Assess the morphology of the erythrocytes.
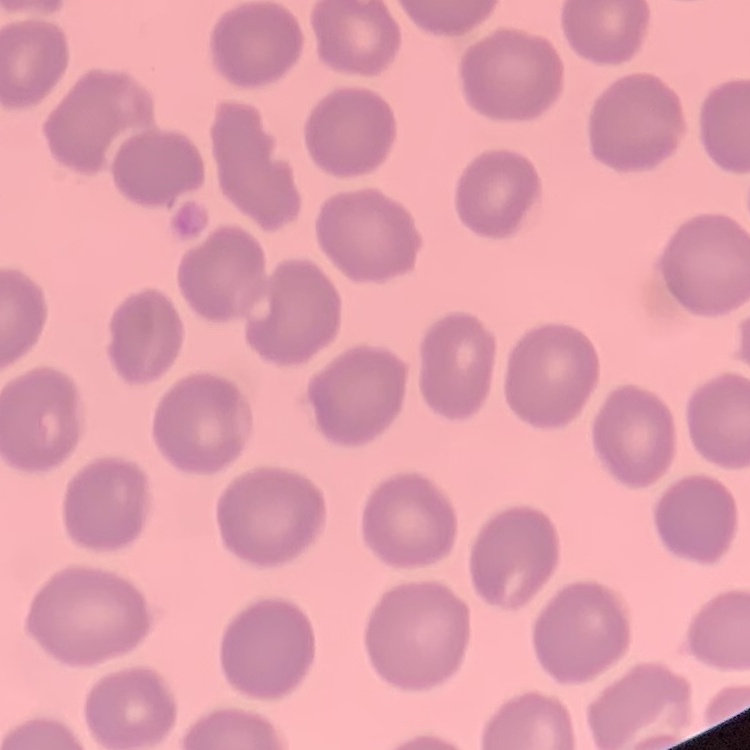

They show no rouleaux formation.

{
  "image_type": "square crop of a larger photomicrograph",
  "stain": "Field's or Giemsa",
  "preparation": "thin blood film"
}